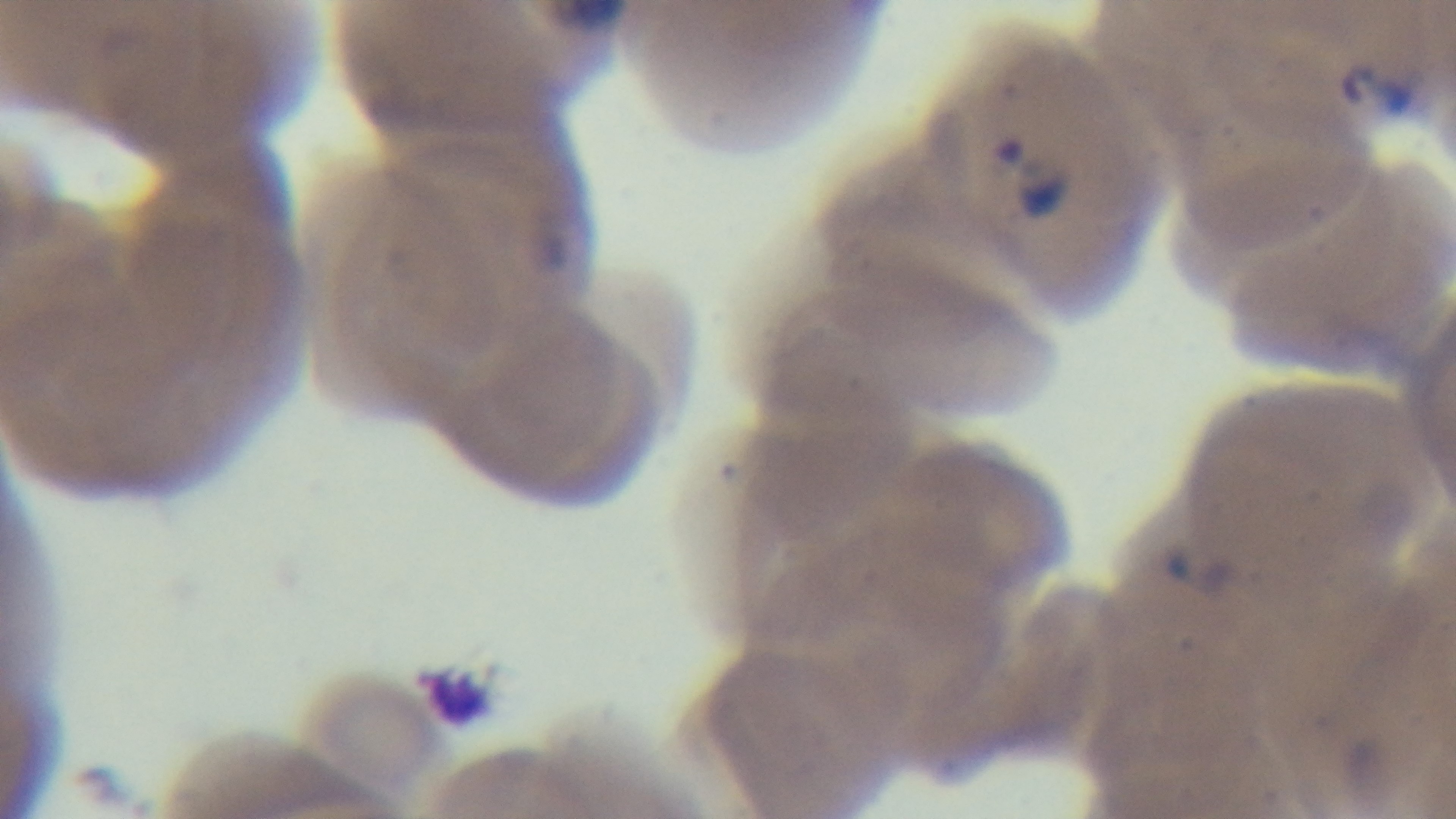

Malaria status: infected. Giemsa stain. One field from the slide. Mounted 4K digital camera. Preparation: thin smear. Oil-immersion objective, 100x. Light microscopy.